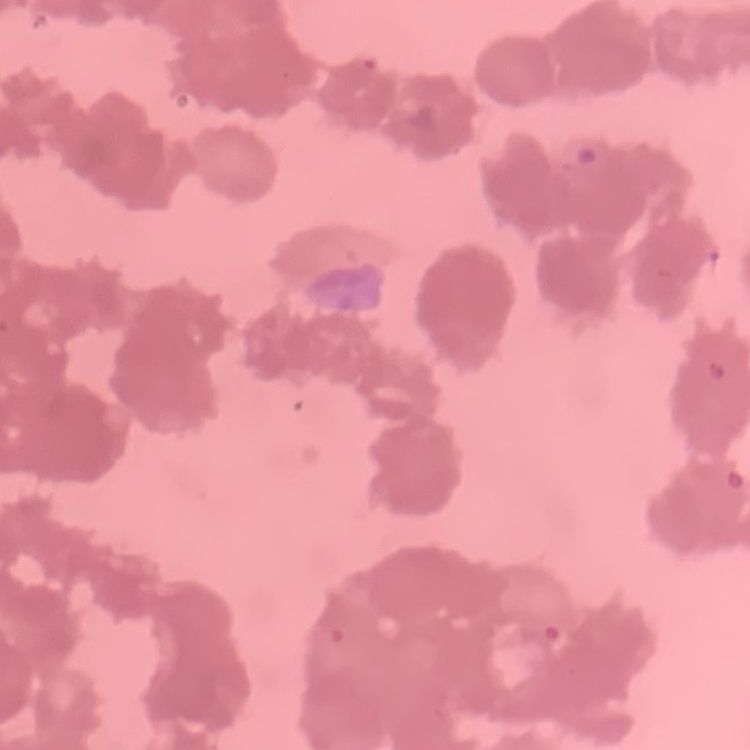
The red blood cells show rouleaux formation. Square crop of a larger photomicrograph. Thin blood film. Stained with either Field's or Giemsa.